Report the malaria status of this cell.
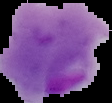

It is parasitized.

Segmented cell region on a black background. Image is 112×103 pixels. From a thin blood smear.